Report the malaria status of this cell.
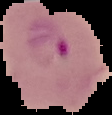

Parasitized.

Cell region segmented out of the field of view; the surrounding area is masked to black. Image is 112×115 pixels. From a thin blood smear.